Assess the morphology of the erythrocytes.
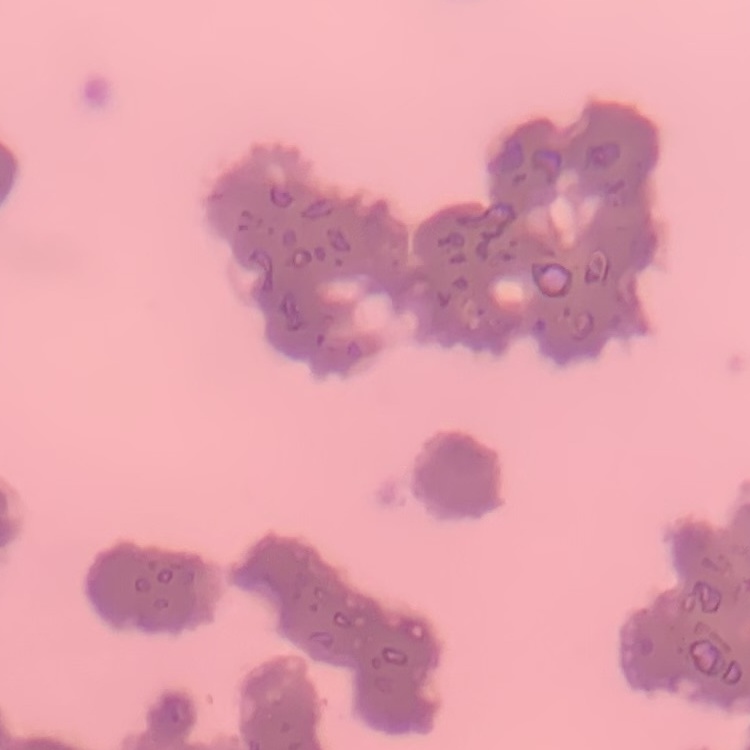
Rouleaux formation.

Square crop of a larger photomicrograph. Field's or Giemsa stain. Thin blood film.